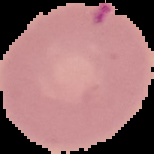

image size = 154×154 pixels
preparation = thin blood smear
image type = segmented cell region on a black background
malaria status = parasitized